Classify this cell by malaria status.
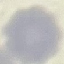

It is uninfected.

Summary:
  - Stain: Giemsa
  - Capture: smartphone through the microscope eyepiece
  - Preparation: thin smear
  - Image type: cell patch, automatically extracted from a larger field of view and resized to 64 × 64 pixels